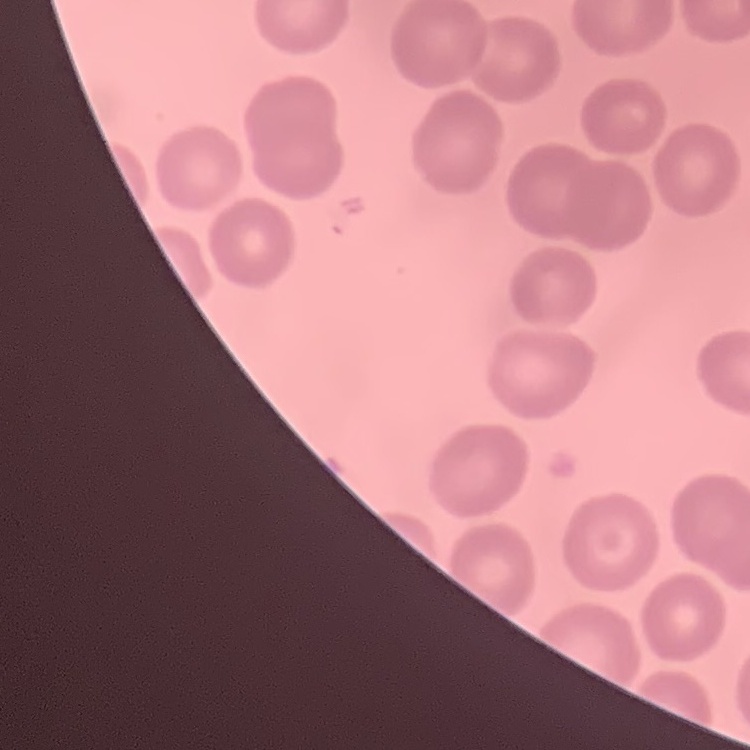 The erythrocytes show no rouleaux formation. Square crop of a larger photomicrograph. Field's or Giemsa stain. Thin peripheral smear.